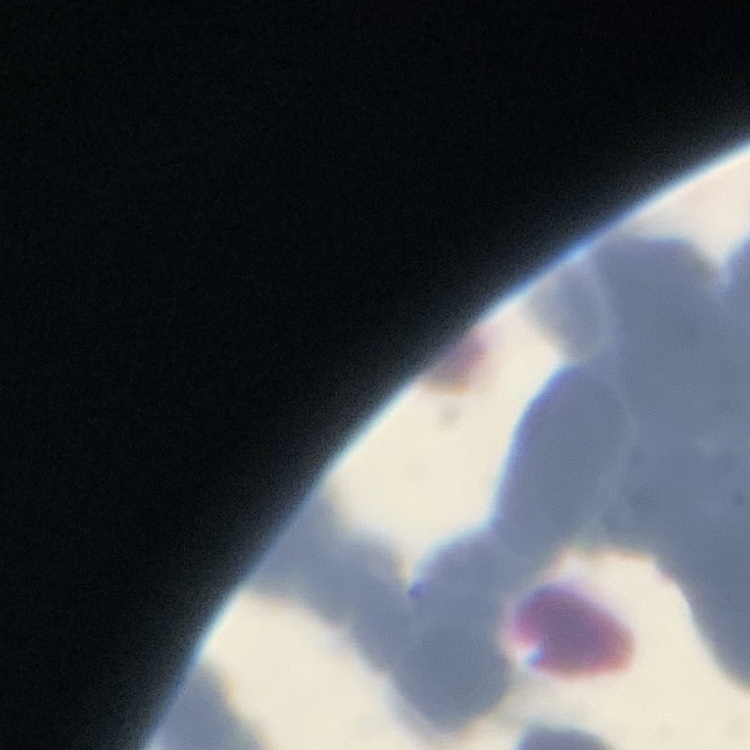

{
  "erythrocyte_morphology": "rouleaux formation",
  "image_type": "one tile cut from a larger photomicrograph",
  "stain": "Field's or Giemsa",
  "preparation": "thin blood film"
}